Evaluate for parasitized red blood cells.
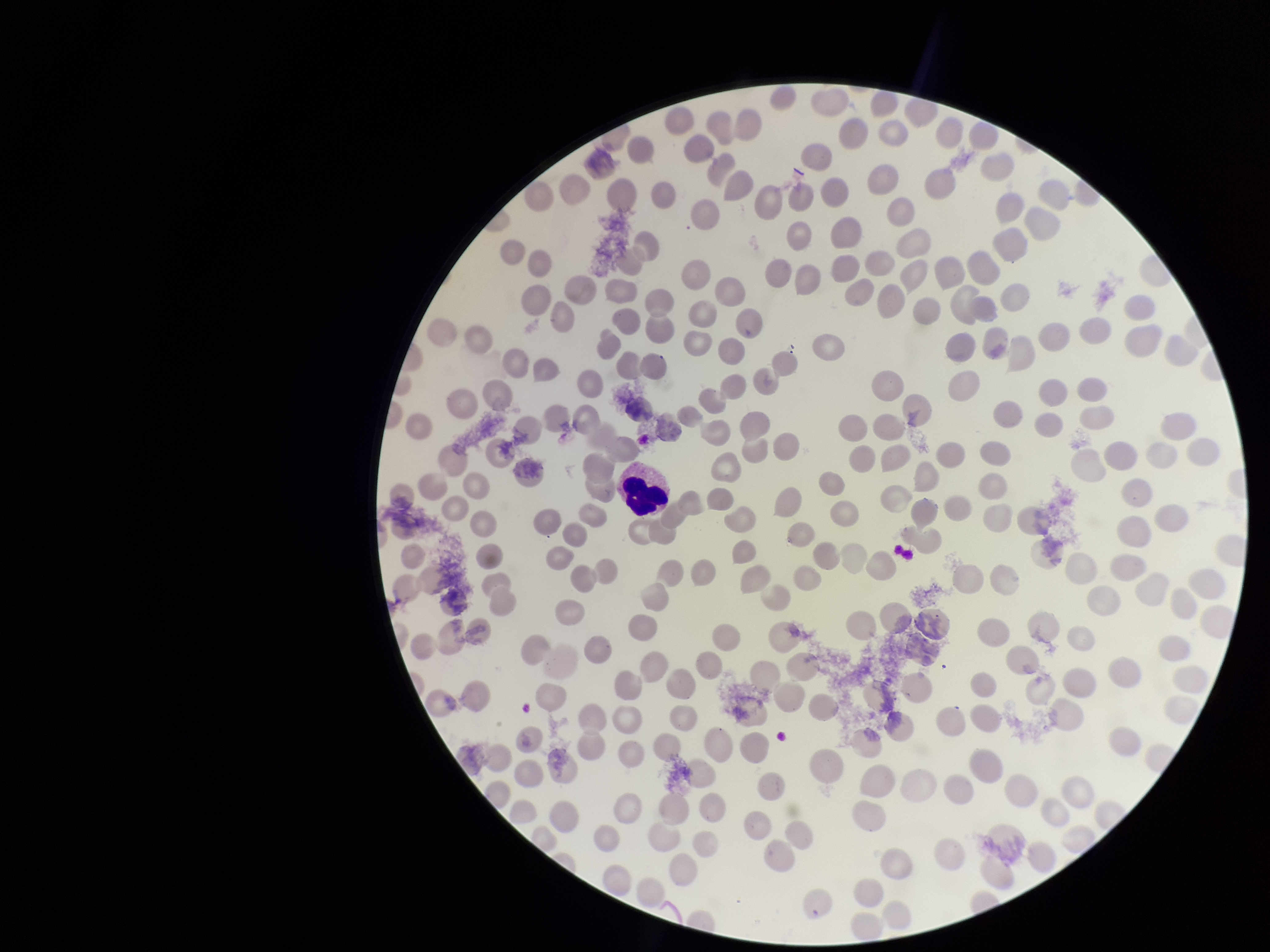
None detected.

{
  "parasitized_red_blood_cell_count": 0,
  "preparation": "thin smear",
  "capture": "smartphone photograph through the microscope eyepiece",
  "image_size": "1270×952 pixels",
  "red_blood_cell_count": 213,
  "stain": "Giemsa",
  "patient_malaria_status": "negative",
  "field_of_view": "one from this slide"
}